Identify the cell.
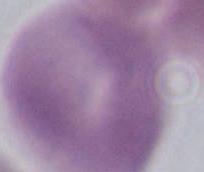

An erythrocyte.

{
  "modality": "photomicrograph",
  "magnification": "1000x"
}